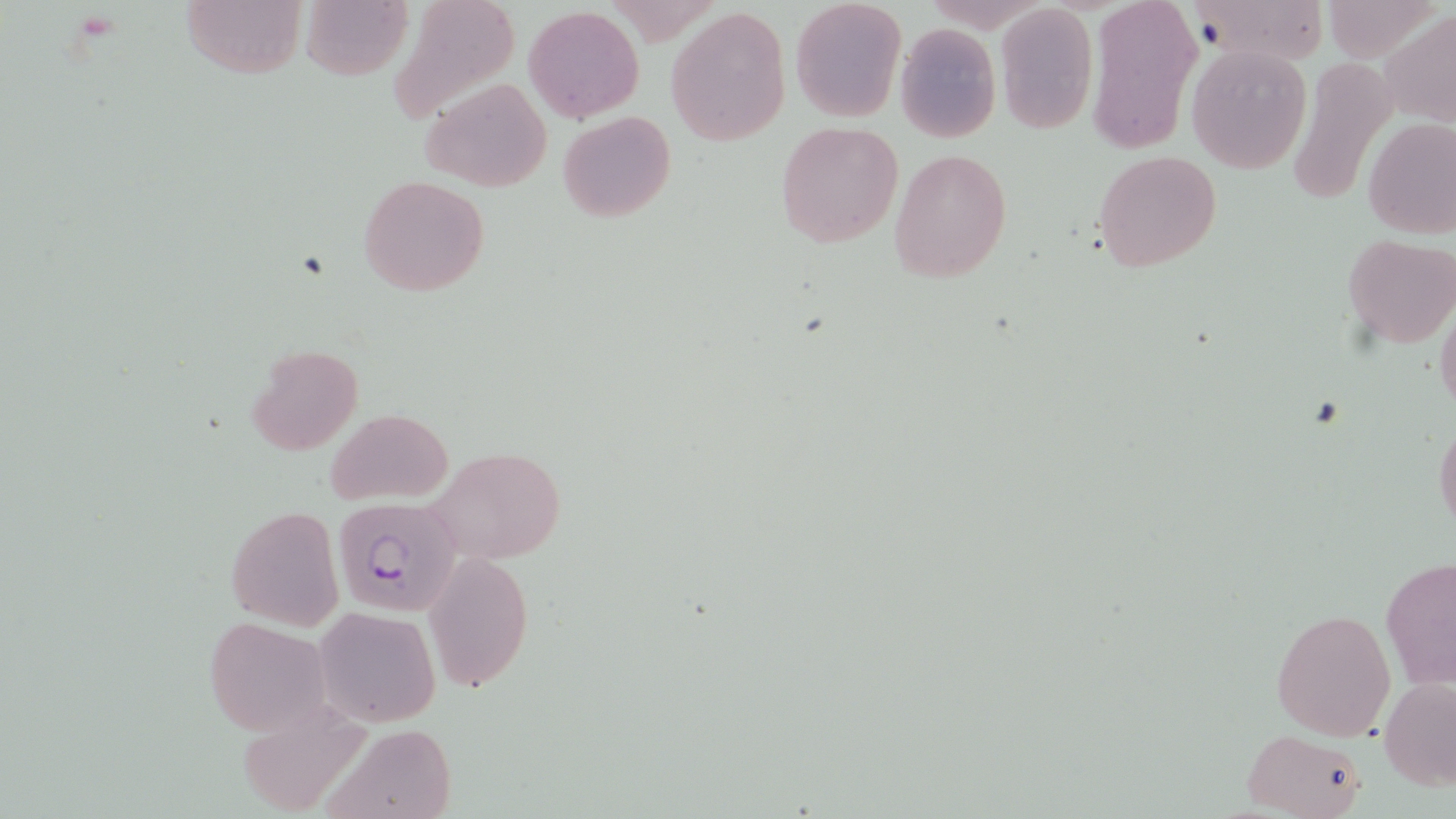
{
  "slide_level_diagnosis": "Plasmodium falciparum",
  "stain": "May-Grünwald-Giemsa",
  "magnification": "1000x",
  "uninfected_red_blood_cell_locations": "approximate bounding boxes as [x1, y1, x2, y2] in pixels: [179, 0, 306, 80], [387, 0, 521, 123], [1086, 0, 1202, 156], [1197, 0, 1323, 66], [301, 1, 411, 81], [789, 1, 905, 120], [994, 3, 1098, 133], [525, 6, 644, 122], [665, 6, 790, 146], [1382, 11, 1455, 129], [895, 23, 1001, 143], [1186, 42, 1312, 173], [1285, 56, 1395, 208], [421, 78, 551, 190], [558, 110, 675, 223], [1362, 116, 1456, 238], [774, 120, 905, 250], [890, 147, 1013, 285], [1092, 149, 1223, 273], [358, 174, 490, 297], [1341, 234, 1456, 349], [1435, 301, 1456, 417], [245, 344, 363, 456], [325, 408, 451, 505], [1433, 419, 1456, 533], [427, 447, 571, 566], [225, 505, 344, 630], [425, 551, 533, 690], [1380, 555, 1455, 692], [1271, 607, 1395, 741], [316, 608, 441, 726], [203, 614, 334, 737], [1379, 676, 1456, 792], [320, 722, 459, 819], [1241, 728, 1367, 819]",
  "preparation": "thin blood film",
  "image_size": "1456×819 pixels",
  "field_of_view": "one of a larger specimen",
  "modality": "optical microscopy",
  "plasmodium_falciparum_infected_red_blood_cell_locations": "approximate bounding boxes as [x1, y1, x2, y2] in pixels: [339, 500, 465, 619]"
}